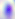

Summary:
  - Modality: photomicrograph
  - Magnification: 400x
  - Identification: Toxoplasma gondii